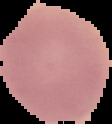
{
  "image_type": "cell region segmented out of the field of view; surrounding area masked to black",
  "preparation": "thin blood smear",
  "image_size": "112×124 pixels",
  "result": "no malaria parasites detected"
}